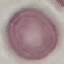
result = no malaria parasites seen
image type = cell patch, automatically extracted from a larger field of view and resized to 64 × 64 pixels
preparation = thin blood film
stain = Giemsa
capture = smartphone through the microscope eyepiece